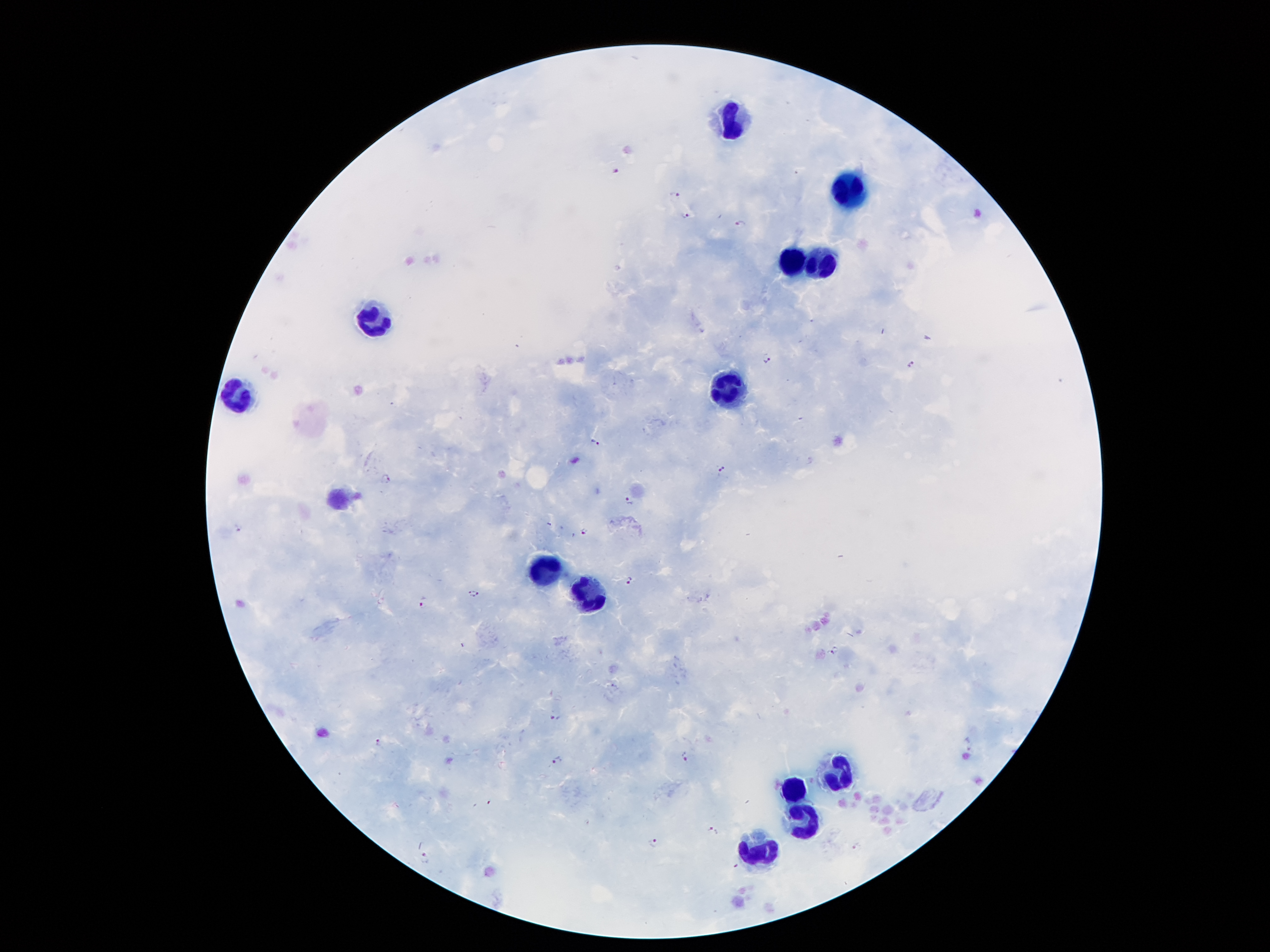
Approximate centers as {x, y} in pixels. Leukocyte locations: {733, 120}, {850, 189}, {792, 261}, {823, 266}, {375, 317}, {724, 388}, {239, 397}, {544, 567}, {589, 596}, {838, 772}, {791, 788}, {808, 821}, {760, 853}. Plasmodium parasite locations: {615, 169}, {674, 192}, {686, 216}, {738, 223}, {765, 359}, {912, 364}, {595, 441}, {723, 469}, {387, 479}, {630, 500}, {238, 528}, {584, 532}, {630, 579}, {474, 593}, {423, 606}, {834, 649}, {553, 717}, {378, 744}, {684, 756}, {557, 761}, {712, 832}, {654, 844}, {856, 847}, {424, 858}. 100x magnification. Image is 1270×952 pixels. Thick blood smear. Patient malaria status: infected with Plasmodium falciparum. Single field of view. Photographed through the microscope eyepiece with a smartphone camera. Giemsa-stained preparation.